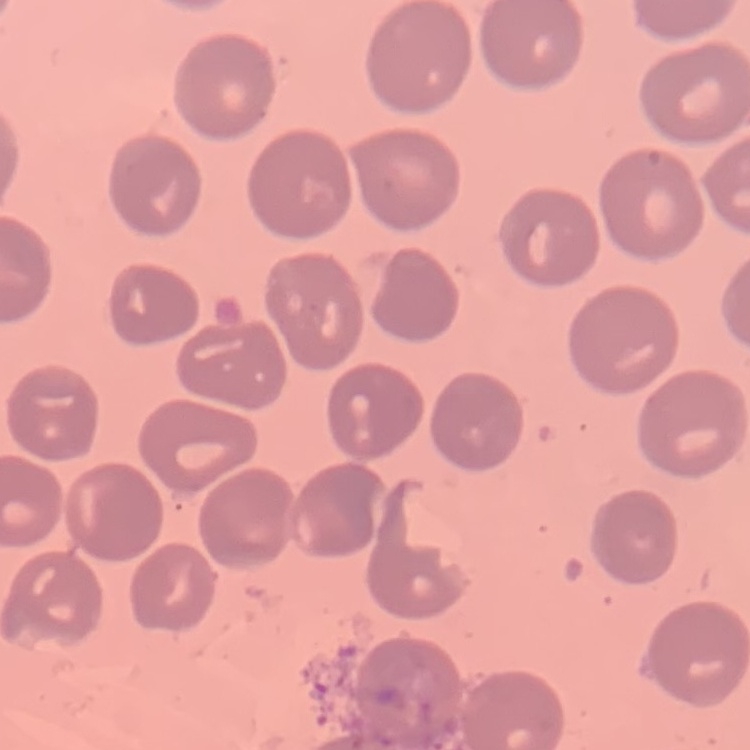

The erythrocytes show no rouleaux formation. Thin blood film. Square crop of a larger photomicrograph. Field's or Giemsa stain.